State the preparation type.
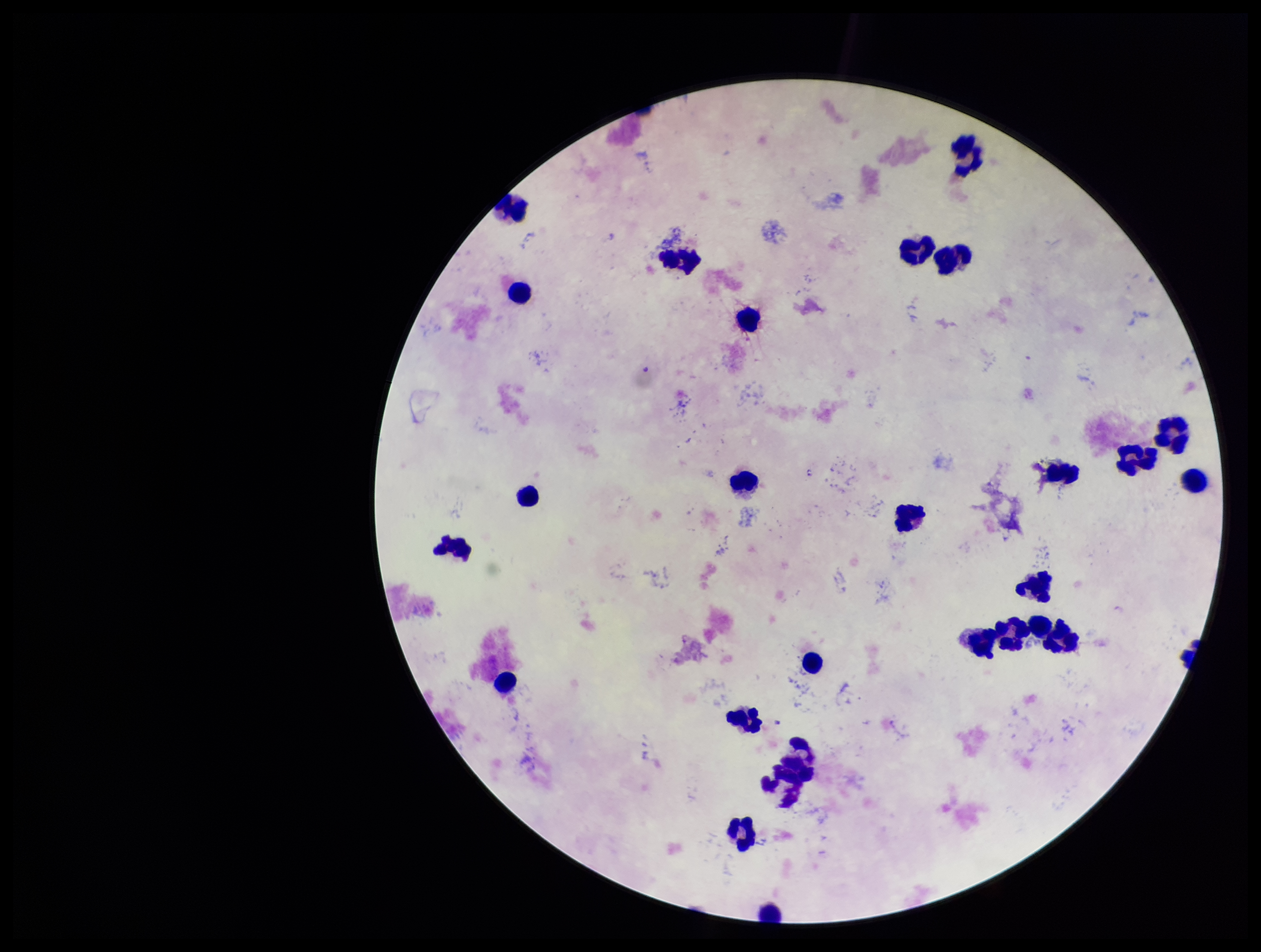

Thick.

Plasmodium parasites = none seen
parasite count = 0
capture = smartphone photograph through the microscope eyepiece
leukocyte count = 26
image size = 1261×952 pixels
stain = Giemsa
field of view = one from this slide
patient malaria status = negative